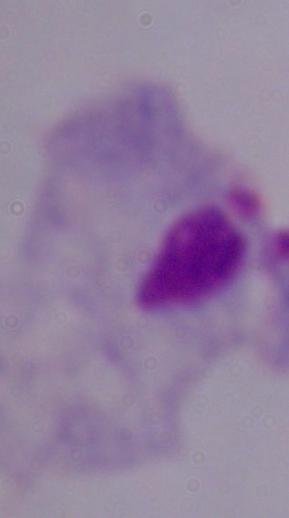 Micrograph. 1000x magnification. A trichomonad is seen.